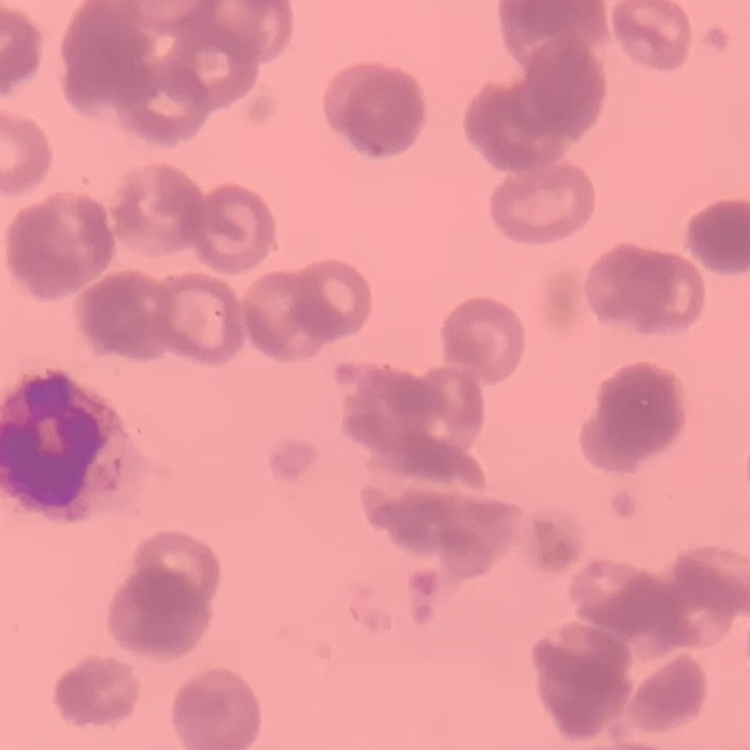

red blood cell morphology = rouleaux formation
preparation = thin blood film
stain = Field's or Giemsa
image type = square crop of a larger photomicrograph